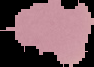
From a thin blood smear. Result: no Plasmodium parasites seen. Cell region segmented out of the field of view; the surrounding area is masked to black. Image is 94×67 pixels.